Outline each Plasmodium malariae-infected red blood cell.
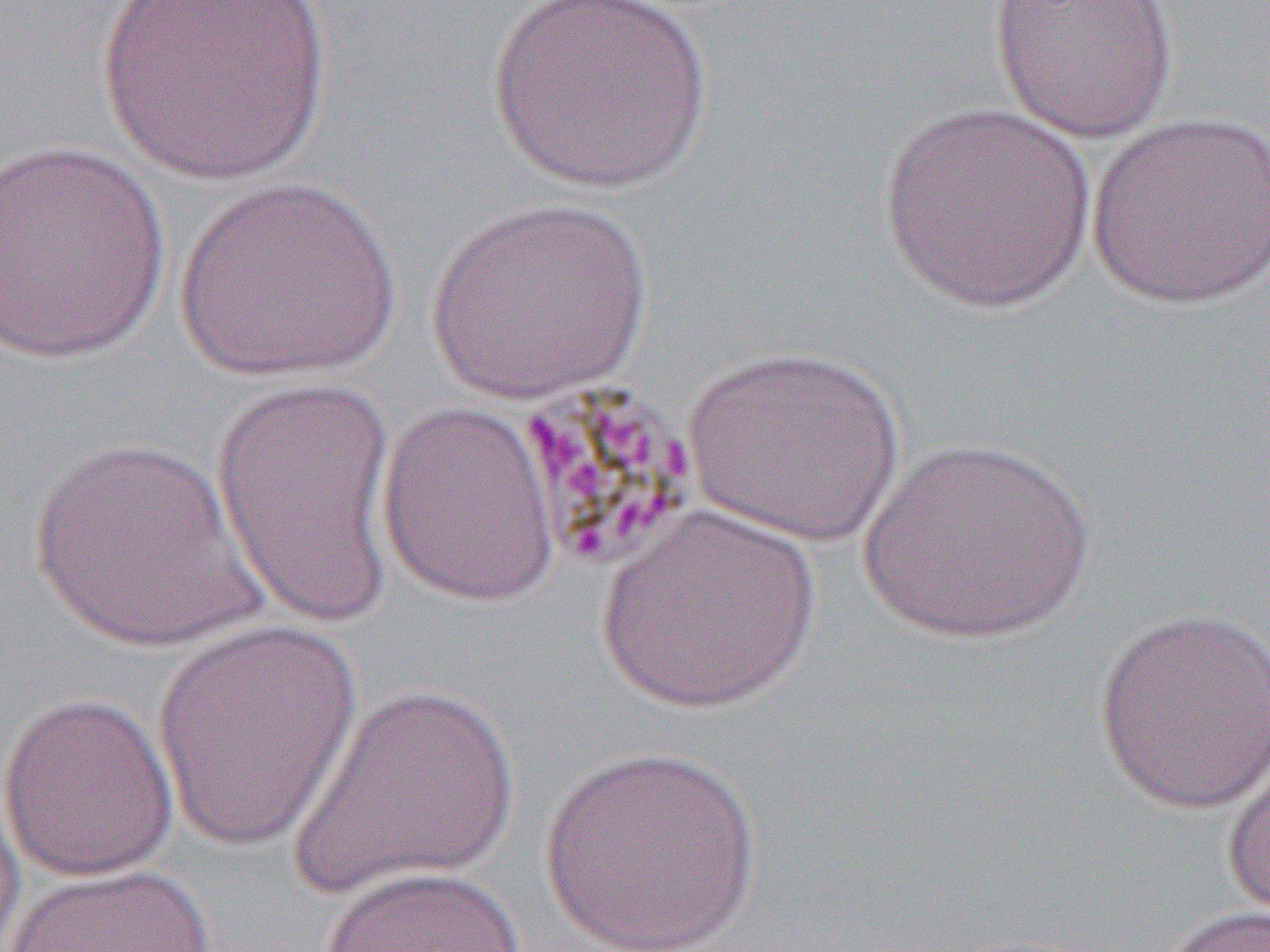
Approximate bounding boxes as named x1/y1/x2/y2 corners in pixels.
Plasmodium malariae-infected red blood cells: (x1=517, y1=379, x2=700, y2=572).

slide-level diagnosis = Plasmodium malariae
magnification = 1000x
field of view = single
image size = 1270×952 pixels
preparation = thin blood film
modality = light microscopy
uninfected red blood cell locations = approximate bounding boxes as named x1/y1/x2/y2 corners in pixels: (x1=94, y1=0, x2=336, y2=187), (x1=487, y1=0, x2=713, y2=195), (x1=988, y1=0, x2=1181, y2=144), (x1=877, y1=100, x2=1100, y2=314), (x1=1086, y1=111, x2=1270, y2=310), (x1=0, y1=140, x2=172, y2=368), (x1=175, y1=177, x2=401, y2=384), (x1=426, y1=197, x2=652, y2=404), (x1=684, y1=344, x2=905, y2=547), (x1=211, y1=371, x2=401, y2=636), (x1=375, y1=401, x2=563, y2=607), (x1=853, y1=435, x2=1100, y2=648), (x1=23, y1=436, x2=269, y2=658), (x1=596, y1=504, x2=822, y2=714), (x1=1092, y1=607, x2=1270, y2=816), (x1=148, y1=619, x2=367, y2=853), (x1=289, y1=682, x2=522, y2=904), (x1=0, y1=691, x2=180, y2=883), (x1=1221, y1=745, x2=1270, y2=922), (x1=538, y1=746, x2=762, y2=952), (x1=0, y1=767, x2=27, y2=952), (x1=4, y1=861, x2=217, y2=951), (x1=318, y1=865, x2=526, y2=952), (x1=1153, y1=903, x2=1270, y2=952)